Report the malaria status of this cell.
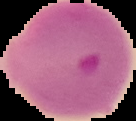
Parasitized.

image type = segmented cell region on a black background
image size = 136×121 pixels
preparation = thin blood smear